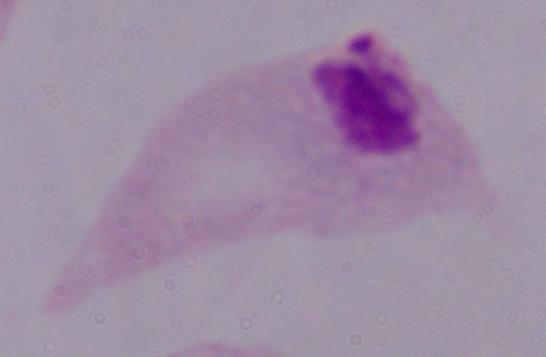
{
  "modality": "photomicrograph",
  "identification": "trichomonad",
  "magnification": "1000x"
}